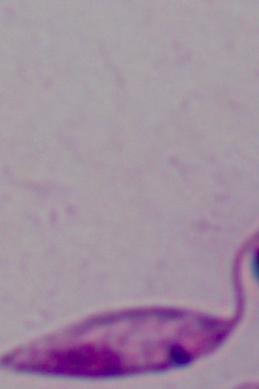

magnification = 1000x
identification = Leishmania
modality = micrograph